Identify the parasite.
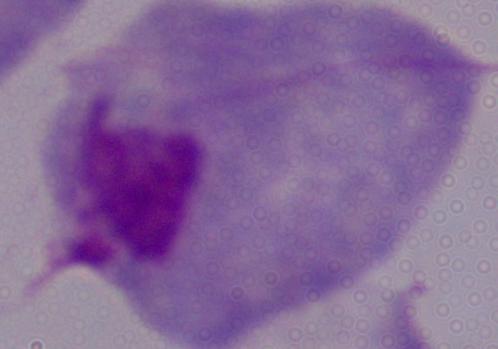

This is a trichomonad.

1000x magnification. Photomicrograph.